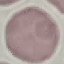
result = no malaria parasites detected
stain = Giemsa
image type = cell patch, automatically extracted from a larger field of view and resized to 64 × 64 pixels
capture = smartphone camera at the microscope eyepiece
preparation = thin smear